Classify this cell by malaria status.
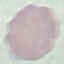

It is uninfected.

preparation: thin blood smear
capture: smartphone camera at the microscope eyepiece
image_type: cell patch, automatically extracted from a larger field of view and resized to 64 × 64 pixels
stain: Giemsa